Identify the blood parasite species.
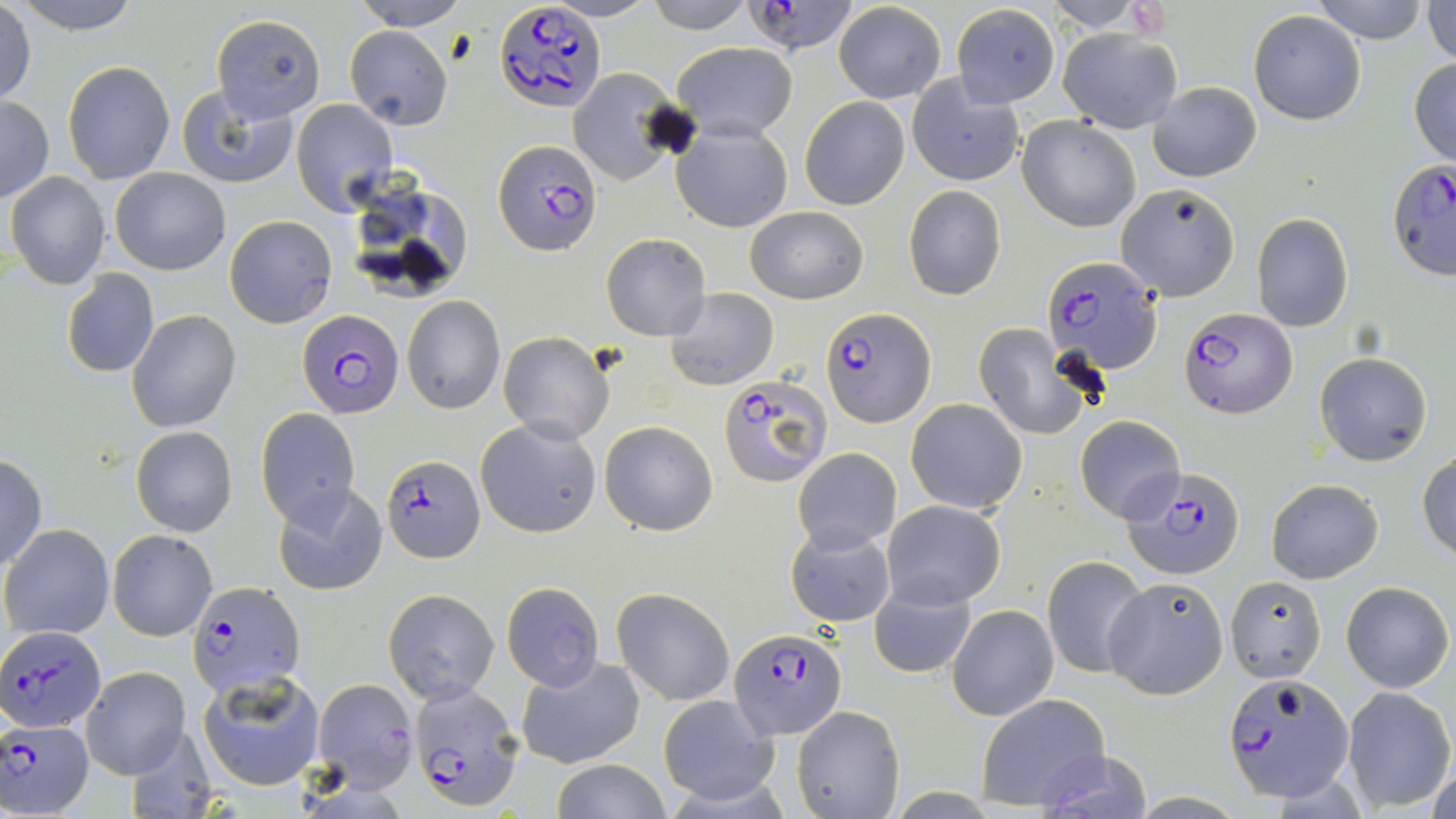
Plasmodium falciparum.

Summary:
  - Coordinate format: approximate bounding boxes as named x1/y1/x2/y2 corners in pixels
  - Plasmodium falciparum-infected red blood cell locations: (x1=745, y1=2, x2=858, y2=56), (x1=495, y1=3, x2=608, y2=114), (x1=494, y1=140, x2=603, y2=258), (x1=1387, y1=156, x2=1454, y2=280), (x1=1043, y1=256, x2=1164, y2=377), (x1=1180, y1=307, x2=1297, y2=420), (x1=300, y1=308, x2=402, y2=418), (x1=822, y1=309, x2=936, y2=427), (x1=718, y1=375, x2=832, y2=486), (x1=380, y1=457, x2=483, y2=562), (x1=1124, y1=467, x2=1244, y2=579), (x1=187, y1=580, x2=305, y2=698), (x1=0, y1=625, x2=105, y2=732), (x1=728, y1=627, x2=847, y2=740), (x1=1226, y1=672, x2=1355, y2=801), (x1=407, y1=679, x2=522, y2=810), (x1=2, y1=719, x2=94, y2=817)
  - Uninfected red blood cell locations: (x1=11, y1=0, x2=146, y2=34), (x1=348, y1=0, x2=473, y2=30), (x1=644, y1=0, x2=757, y2=33), (x1=1048, y1=0, x2=1150, y2=31), (x1=1310, y1=0, x2=1432, y2=44), (x1=1423, y1=0, x2=1456, y2=65), (x1=833, y1=2, x2=946, y2=103), (x1=950, y1=4, x2=1060, y2=107), (x1=1, y1=5, x2=36, y2=106), (x1=1248, y1=9, x2=1365, y2=124), (x1=210, y1=15, x2=325, y2=124), (x1=345, y1=25, x2=453, y2=131), (x1=1058, y1=28, x2=1182, y2=133), (x1=671, y1=40, x2=799, y2=141), (x1=1409, y1=56, x2=1456, y2=165), (x1=62, y1=60, x2=174, y2=184), (x1=567, y1=68, x2=681, y2=184), (x1=908, y1=74, x2=1025, y2=188), (x1=1148, y1=81, x2=1261, y2=183), (x1=176, y1=84, x2=299, y2=191), (x1=804, y1=87, x2=1022, y2=197), (x1=0, y1=94, x2=53, y2=203), (x1=800, y1=95, x2=909, y2=209), (x1=291, y1=99, x2=397, y2=214), (x1=1017, y1=116, x2=1143, y2=231), (x1=672, y1=119, x2=793, y2=232), (x1=110, y1=168, x2=230, y2=275), (x1=5, y1=171, x2=110, y2=289), (x1=1114, y1=182, x2=1240, y2=302), (x1=903, y1=185, x2=1006, y2=302), (x1=745, y1=205, x2=868, y2=304), (x1=1251, y1=212, x2=1355, y2=333), (x1=225, y1=216, x2=337, y2=327), (x1=602, y1=233, x2=711, y2=341), (x1=60, y1=269, x2=160, y2=378), (x1=666, y1=287, x2=778, y2=390), (x1=402, y1=296, x2=505, y2=415), (x1=126, y1=309, x2=241, y2=432), (x1=976, y1=323, x2=1094, y2=440), (x1=497, y1=331, x2=615, y2=444), (x1=1314, y1=353, x2=1432, y2=465), (x1=905, y1=399, x2=1028, y2=513), (x1=256, y1=408, x2=360, y2=530), (x1=1075, y1=415, x2=1185, y2=524), (x1=474, y1=416, x2=603, y2=538), (x1=599, y1=420, x2=718, y2=536), (x1=132, y1=426, x2=238, y2=536), (x1=792, y1=448, x2=901, y2=555), (x1=1418, y1=451, x2=1456, y2=561), (x1=0, y1=454, x2=48, y2=569), (x1=1266, y1=478, x2=1383, y2=583), (x1=274, y1=483, x2=387, y2=597), (x1=881, y1=500, x2=1005, y2=610), (x1=2, y1=523, x2=115, y2=639), (x1=787, y1=526, x2=895, y2=629), (x1=108, y1=529, x2=216, y2=640), (x1=1042, y1=555, x2=1151, y2=677), (x1=1104, y1=575, x2=1229, y2=699), (x1=1224, y1=575, x2=1327, y2=685), (x1=1339, y1=579, x2=1453, y2=692), (x1=868, y1=581, x2=977, y2=679), (x1=501, y1=582, x2=605, y2=690), (x1=613, y1=588, x2=735, y2=706), (x1=384, y1=589, x2=499, y2=705), (x1=948, y1=604, x2=1059, y2=720), (x1=516, y1=654, x2=646, y2=768), (x1=80, y1=666, x2=190, y2=778), (x1=200, y1=672, x2=324, y2=790), (x1=314, y1=677, x2=418, y2=792), (x1=1342, y1=686, x2=1455, y2=810), (x1=656, y1=694, x2=778, y2=806), (x1=977, y1=694, x2=1112, y2=810), (x1=791, y1=705, x2=903, y2=819), (x1=123, y1=724, x2=217, y2=819), (x1=1030, y1=748, x2=1158, y2=819), (x1=548, y1=759, x2=675, y2=818)
  - Image size: 1456×819 pixels
  - Modality: light microscopy
  - Magnification: 1000x
  - Field of view: single
  - Stain: May-Grünwald-Giemsa
  - Preparation: thin blood film